Point out each Plasmodium parasite.
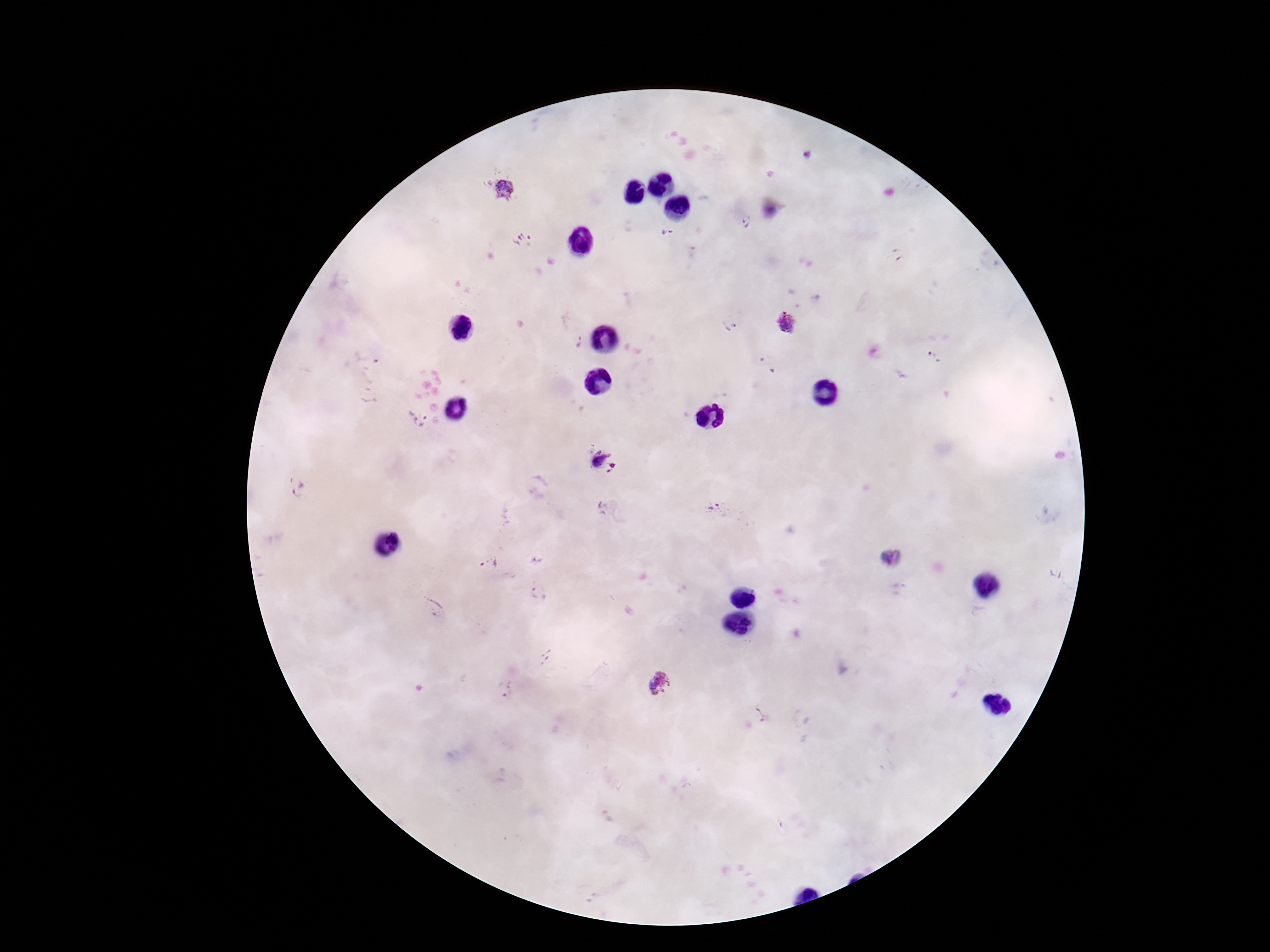

Approximate object centers, in pixels from the top-left corner.
Plasmodium parasites: (x=808, y=154), (x=505, y=190), (x=747, y=223), (x=666, y=233), (x=524, y=241), (x=898, y=256), (x=786, y=324), (x=729, y=326), (x=579, y=341), (x=935, y=358), (x=766, y=366), (x=417, y=417), (x=597, y=460), (x=299, y=491), (x=713, y=509), (x=892, y=558), (x=491, y=564), (x=540, y=592), (x=548, y=660), (x=660, y=683), (x=508, y=691), (x=761, y=715).

patient malaria status = positive
stain = Giemsa
capture = smartphone camera through the microscope eyepiece
magnification = 100x
field of view = one from this slide
image size = 1270×952 pixels
preparation = thick blood film